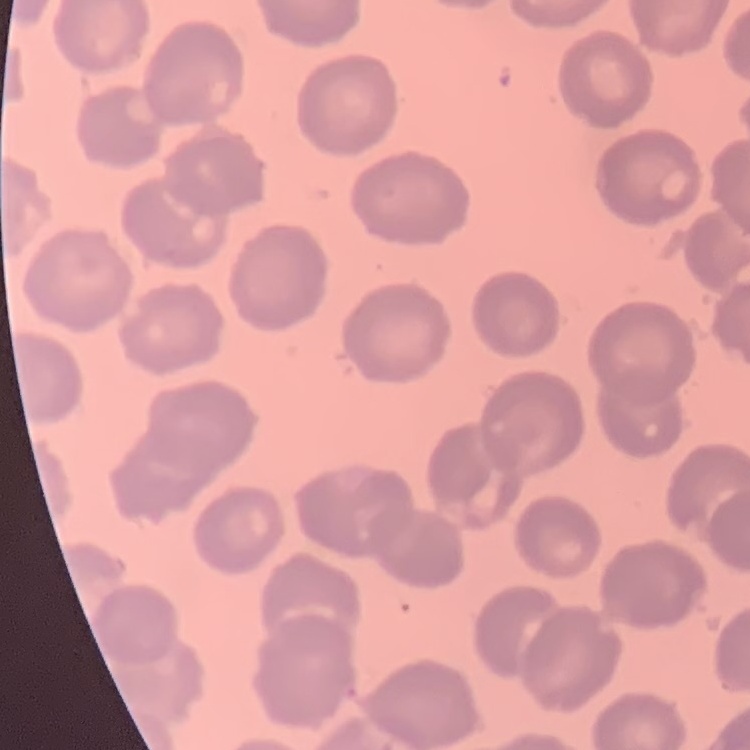

red blood cell morphology = no rouleaux formation
preparation = thin blood film
image type = square crop of a larger photomicrograph
stain = Field's or Giemsa